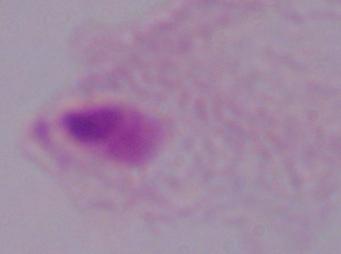

Summary:
  - Modality: photomicrograph
  - Magnification: 1000x
  - Identification: trichomonad